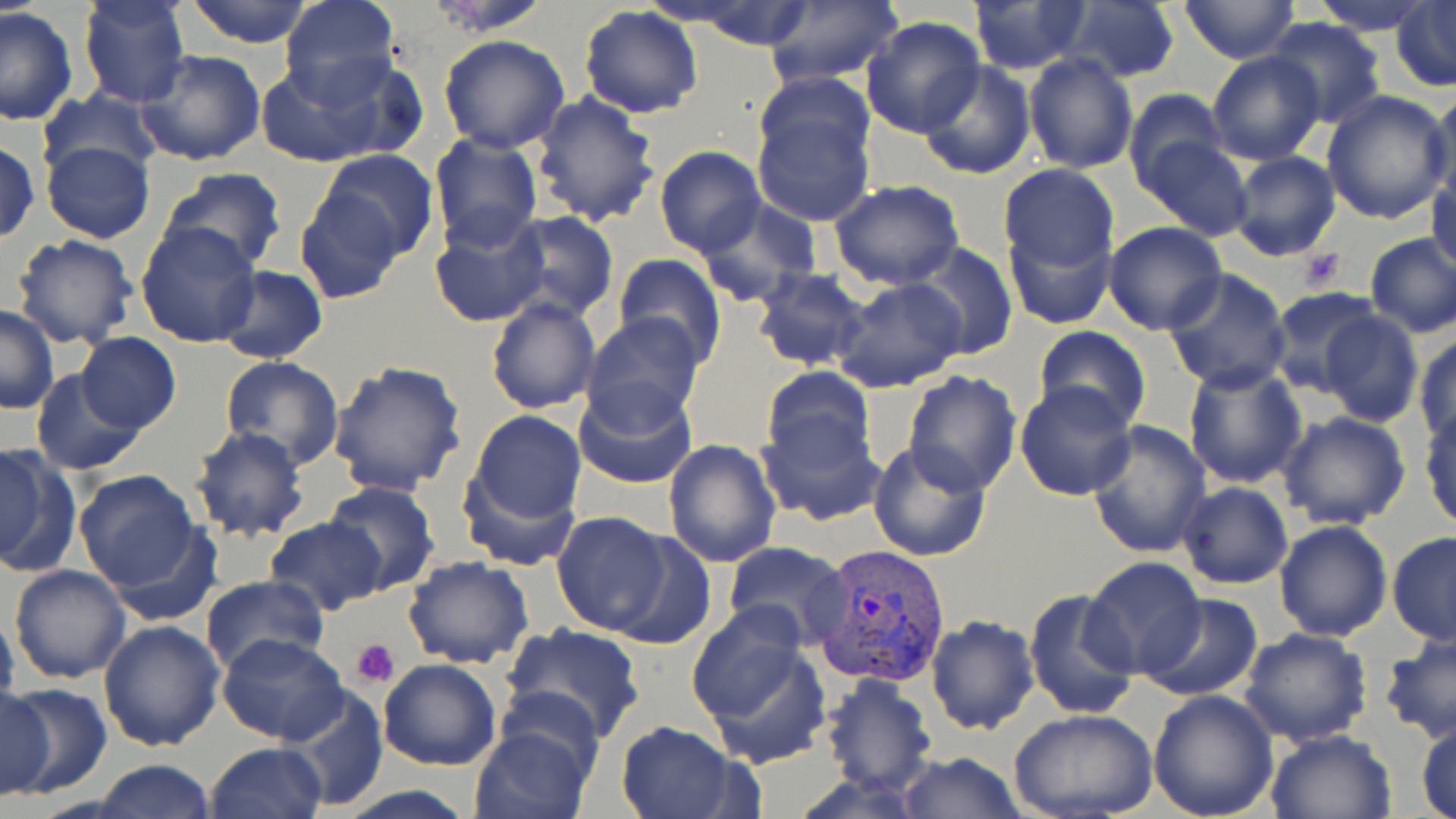
slide_level_diagnosis: Plasmodium vivax
stain: May-Grünwald-Giemsa
plasmodium_vivax_infected_red_blood_cell_locations: 'approximate bounding boxes as (x1,y1)-(x2,y2) corner pairs in pixels: (812,544)-(952,689)'
platelet_locations: 'approximate bounding boxes as (x1,y1)-(x2,y2) corner pairs in pixels: (1297,250)-(1348,289), (350,637)-(401,689)'
magnification: 1000x
image_size: 1456×819 pixels
preparation: thin blood smear
uninfected_red_blood_cell_locations: 'approximate bounding boxes as (x1,y1)-(x2,y2) corner pairs in pixels: (184,0)-(314,48), (277,0)-(400,104), (422,0)-(553,37), (665,0)-(819,50), (759,0)-(904,90), (1058,0)-(1182,85), (1179,0)-(1298,64), (1309,0)-(1437,34), (76,1)-(192,108), (1390,1)-(1456,89), (968,2)-(1091,74), (578,5)-(703,118), (0,7)-(78,126), (859,16)-(985,138), (1262,17)-(1385,127), (437,35)-(570,153), (135,48)-(267,167), (259,50)-(410,168), (1206,51)-(1326,165), (1023,53)-(1138,174), (918,61)-(1038,181), (752,71)-(873,169), (1428,88)-(1456,207), (1123,89)-(1226,192), (38,90)-(163,186), (529,91)-(660,227), (1320,91)-(1453,225), (748,98)-(876,227), (426,133)-(543,252), (1140,136)-(1254,238), (0,138)-(41,245), (40,139)-(155,245), (655,146)-(767,258), (315,147)-(439,262), (1226,150)-(1342,261), (1428,159)-(1456,277), (999,164)-(1118,276), (158,167)-(288,274), (828,179)-(964,289), (294,188)-(408,304), (695,197)-(820,306), (501,210)-(620,323), (429,215)-(547,329), (1005,220)-(1118,329), (1102,221)-(1229,335), (135,222)-(262,348), (1365,234)-(1456,338), (11,235)-(140,352), (908,240)-(1019,361), (613,252)-(726,367), (214,266)-(327,364), (751,266)-(875,372), (1162,268)-(1291,394), (830,277)-(968,394), (1267,288)-(1384,398), (485,296)-(600,415), (0,304)-(59,414), (1319,309)-(1425,427), (583,313)-(706,429), (1033,326)-(1151,434), (1413,331)-(1456,448), (76,332)-(180,433), (219,355)-(345,469), (328,359)-(468,497), (1183,362)-(1307,487), (760,366)-(876,472), (31,368)-(146,475), (900,369)-(1022,497), (573,377)-(697,490), (1014,378)-(1140,501), (755,405)-(885,528), (1420,406)-(1456,531), (461,409)-(587,544), (1276,411)-(1411,531), (1085,419)-(1214,559), (189,426)-(309,542), (663,439)-(781,569), (0,440)-(79,578), (867,442)-(994,563), (73,468)-(208,601), (324,480)-(439,595), (1176,481)-(1293,587), (551,510)-(674,637), (264,517)-(386,617), (1274,518)-(1394,641), (607,528)-(716,649), (1388,530)-(1456,645), (722,541)-(852,645), (402,555)-(535,671), (1081,558)-(1205,678), (8,564)-(130,684), (199,574)-(326,677), (1023,587)-(1144,723), (1136,593)-(1264,701), (685,607)-(832,766), (0,610)-(21,710), (926,615)-(1038,735), (97,619)-(226,753), (499,623)-(648,746), (1238,629)-(1373,748), (217,633)-(350,745), (1378,637)-(1456,744), (378,658)-(501,771), (821,673)-(939,798), (3,684)-(109,797), (281,686)-(388,811), (0,688)-(54,801), (1147,688)-(1279,819), (1009,710)-(1157,819), (1416,720)-(1456,819), (613,721)-(743,819), (469,724)-(593,819), (1265,729)-(1396,817), (204,742)-(327,819), (895,751)-(1025,818), (95,759)-(216,818), (331,784)-(481,819)'
modality: light microscopy
field_of_view: one of a larger specimen